Identify the parasite.
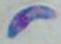
Toxoplasma gondii.

Micrograph. 1000x magnification.